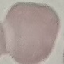
result = no malaria parasites detected
preparation = thin blood film
image type = automatically extracted cell patch, resized to 64 × 64 pixels
capture = smartphone camera at the microscope eyepiece
stain = Giemsa